Give the position of every Plasmodium parasite visible.
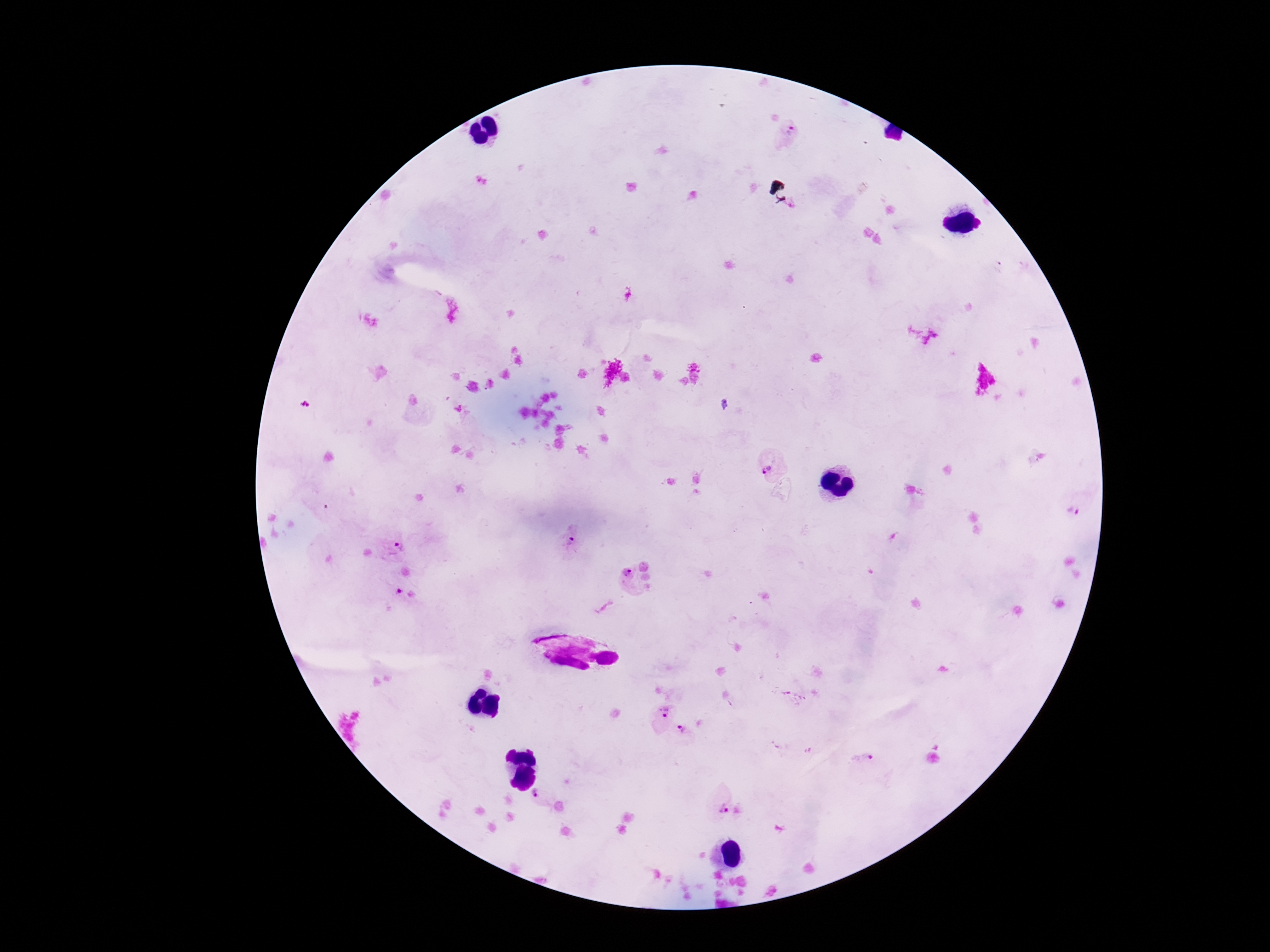

Approximate centers as (x, y) in pixels.
Plasmodium parasites: (790, 133), (772, 465), (1074, 511), (572, 542), (390, 544), (621, 577), (399, 593), (661, 716), (685, 734), (862, 760), (541, 798), (718, 803).

Summary:
  - Capture: smartphone camera through the microscope eyepiece
  - Preparation: thick peripheral-blood smear
  - Magnification: 100x
  - Stain: Giemsa
  - Image size: 1270×952 pixels
  - Patient malaria status: infected
  - Field of view: single